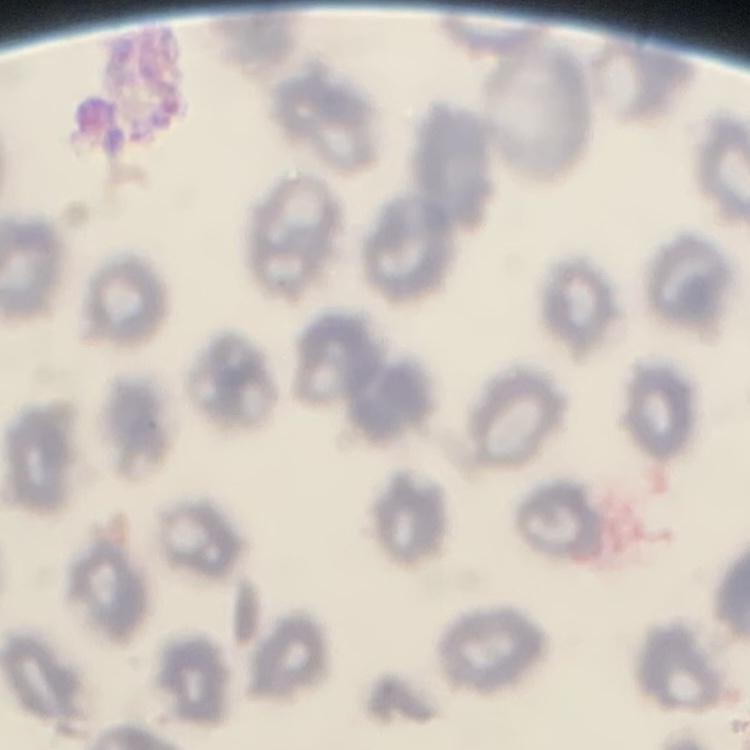
The red blood cells show no rouleaux formation. One tile cut from a larger photomicrograph. Thin peripheral smear. Stained with either Field's or Giemsa.